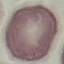
result: no malaria parasites seen
capture: smartphone through the microscope eyepiece
image_type: cell patch, automatically extracted from a larger field of view and resized to 64 × 64 pixels
preparation: thin blood smear
stain: Giemsa